Classify this cell by malaria status.
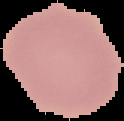
Uninfected.

Summary:
  - Image type: cell region segmented out of the field of view; surrounding area masked to black
  - Preparation: thin blood smear
  - Image size: 124×121 pixels